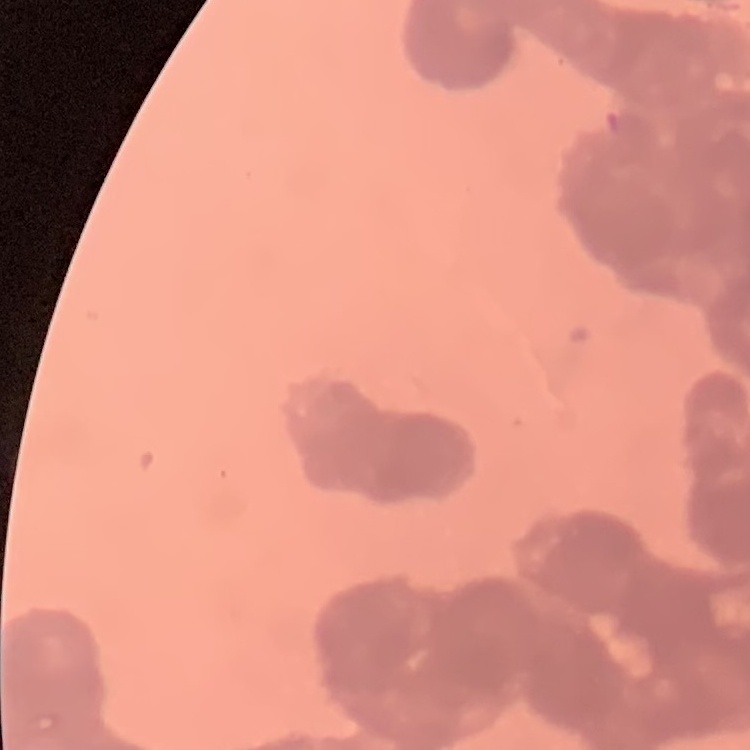

The erythrocytes exhibit rouleaux formation. One tile cut from a larger photomicrograph. Thin blood film. Stained with either Field's or Giemsa.